Locate every Trypanosoma brucei.
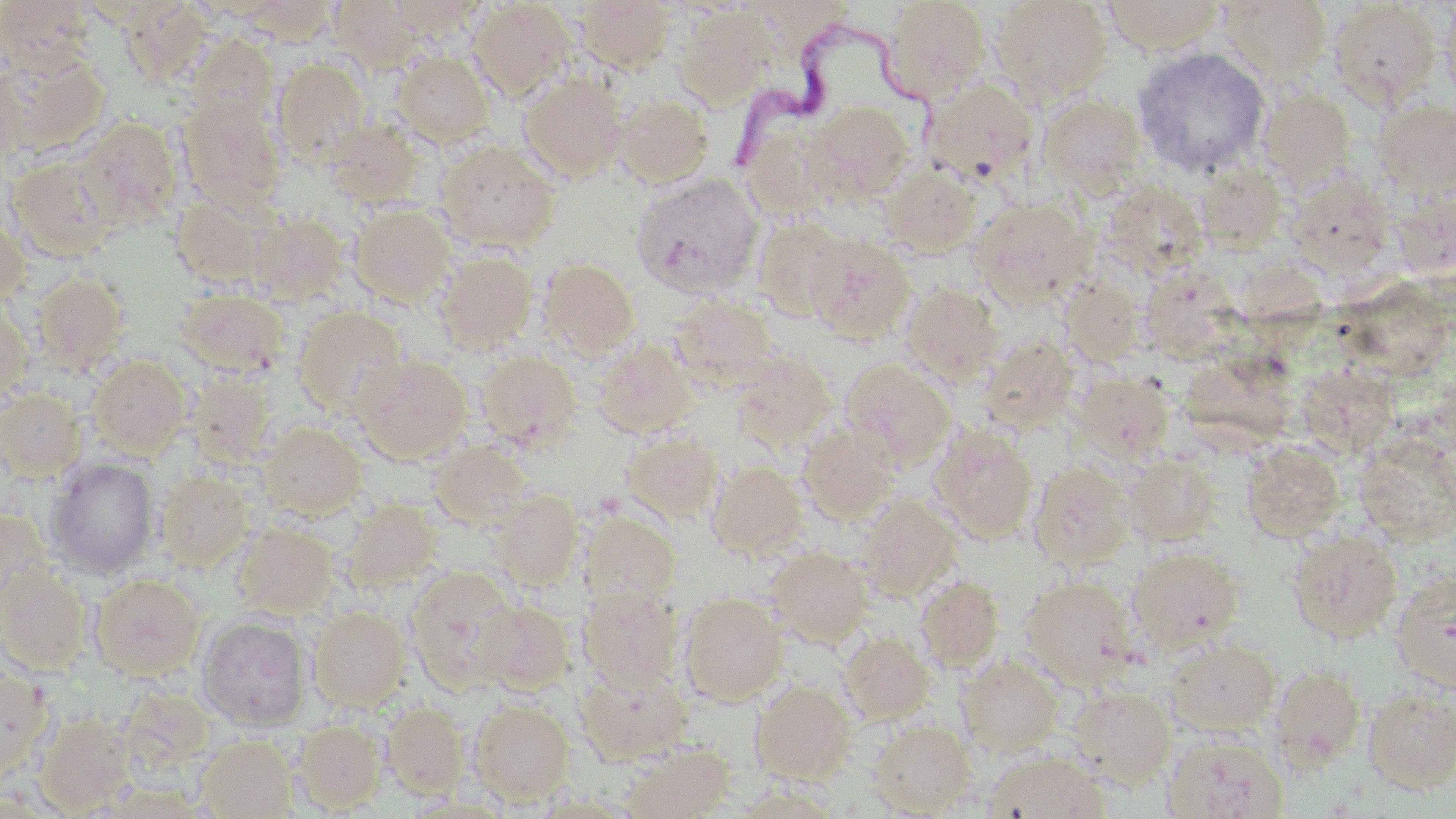

Approximate bounding boxes as [x1, y1, x2, y2] in pixels.
Trypanosoma brucei: [721, 23, 946, 179].

slide-level diagnosis = Trypanosoma brucei
image size = 1456×819 pixels
field of view = one of a larger specimen
uninfected red blood cell locations = approximate bounding boxes as [x1, y1, x2, y2] in pixels: [0, 0, 95, 70], [236, 0, 338, 42], [330, 0, 423, 72], [389, 0, 486, 39], [882, 0, 988, 102], [1102, 0, 1226, 54], [1221, 0, 1332, 80], [469, 1, 575, 101], [574, 1, 675, 72], [992, 1, 1112, 101], [1329, 1, 1440, 106], [1441, 1, 1456, 107], [121, 4, 212, 82], [676, 8, 772, 108], [187, 32, 278, 124], [1132, 47, 1270, 178], [2, 49, 109, 155], [392, 52, 494, 147], [272, 58, 370, 165], [0, 65, 29, 169], [519, 73, 626, 183], [923, 79, 1039, 185], [1259, 89, 1355, 188], [177, 92, 286, 210], [614, 94, 713, 186], [1038, 95, 1147, 194], [1374, 99, 1456, 196], [808, 101, 913, 201], [740, 113, 844, 222], [78, 117, 182, 228], [325, 117, 424, 206], [435, 140, 561, 253], [7, 156, 117, 261], [880, 163, 981, 257], [1197, 163, 1286, 252], [1288, 172, 1394, 271], [631, 173, 763, 296], [1100, 181, 1209, 280], [1392, 190, 1455, 277], [171, 196, 269, 287], [970, 196, 1095, 309], [350, 203, 455, 305], [0, 212, 30, 307], [249, 212, 347, 303], [752, 214, 850, 322], [806, 234, 915, 345], [436, 250, 537, 353], [540, 257, 639, 357], [1141, 267, 1241, 362], [1247, 268, 1330, 350], [33, 272, 129, 371], [1345, 273, 1448, 383], [1061, 277, 1143, 364], [901, 282, 1004, 384], [176, 290, 288, 378], [669, 293, 779, 388], [0, 303, 32, 404], [293, 306, 408, 418], [980, 336, 1078, 432], [594, 339, 699, 439], [1185, 346, 1296, 448], [477, 350, 582, 450], [731, 352, 835, 450], [355, 354, 472, 462], [88, 355, 191, 457], [840, 358, 956, 466], [1296, 367, 1396, 457], [186, 370, 277, 466], [1075, 370, 1174, 459], [0, 389, 87, 480], [259, 421, 366, 519], [798, 422, 900, 522], [931, 426, 1037, 542], [623, 430, 722, 522], [1354, 431, 1455, 544], [429, 440, 532, 529], [1244, 442, 1344, 541], [1124, 455, 1221, 544], [45, 458, 160, 577], [708, 461, 807, 559], [1028, 461, 1135, 569], [156, 469, 253, 571], [493, 490, 582, 589], [856, 493, 960, 603], [342, 498, 442, 591], [0, 507, 51, 611], [580, 510, 680, 606], [235, 523, 336, 617], [1287, 530, 1403, 642], [768, 546, 873, 646], [1127, 546, 1243, 651], [0, 566, 91, 673], [406, 566, 523, 689], [90, 572, 204, 679], [1392, 572, 1456, 692], [916, 575, 1004, 671], [1020, 576, 1138, 688], [578, 584, 682, 689], [679, 591, 787, 703], [479, 601, 575, 694], [309, 606, 409, 709], [196, 616, 310, 730], [839, 631, 934, 724], [1164, 637, 1280, 737], [958, 655, 1064, 757], [577, 662, 693, 762], [0, 663, 53, 782], [1271, 665, 1366, 770], [752, 679, 855, 783], [1070, 684, 1176, 788], [1363, 685, 1456, 792], [469, 699, 575, 805], [383, 702, 468, 798], [36, 712, 136, 814], [294, 719, 386, 812], [869, 719, 976, 816], [1164, 733, 1287, 819], [198, 734, 296, 818], [621, 743, 735, 819], [985, 750, 1109, 818]
preparation = thin blood smear
magnification = 1000x
modality = light microscopy
stain = May-Grünwald-Giemsa